Classify this cell by malaria status.
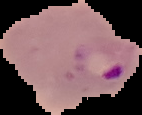
Parasitized.

image size = 142×115 pixels
image type = segmented cell region on a black background
preparation = thin blood smear